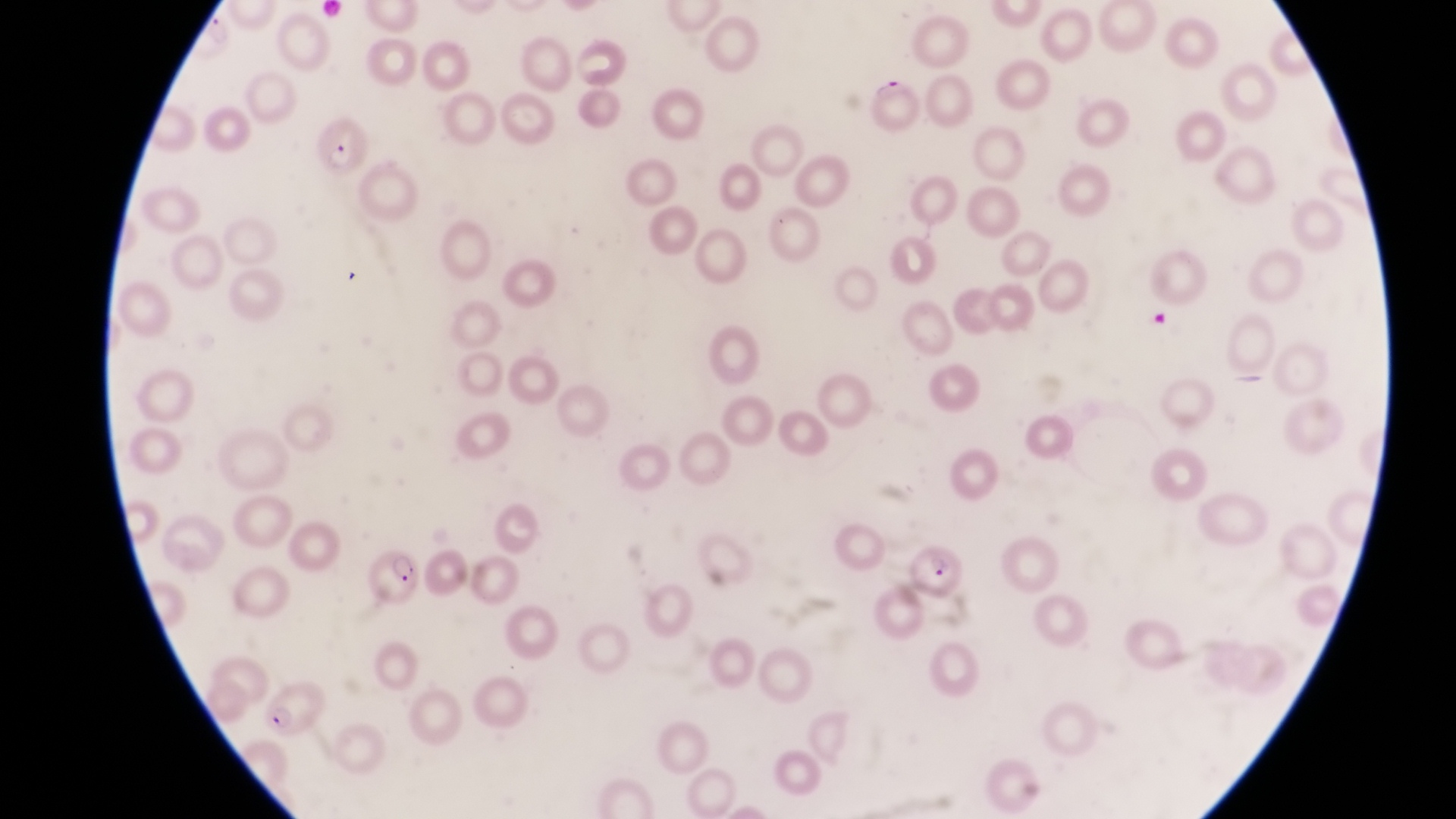
Approximate bounding boxes as (left, top, right, bottom) in pixels.
Summary:
  - Parasitised red blood cell locations: (312, 119, 365, 174), (908, 542, 968, 605), (366, 549, 425, 609), (258, 680, 329, 741)
  - Trophozoite locations: (207, 15, 234, 44)
  - Preparation: thin blood film
  - Capture: smartphone photograph through the eyepiece of an Olympus CX-23 microscope
  - Magnification: 1000x
  - Field of view: single
  - Country: Uganda
  - Image size: 1456×819 pixels